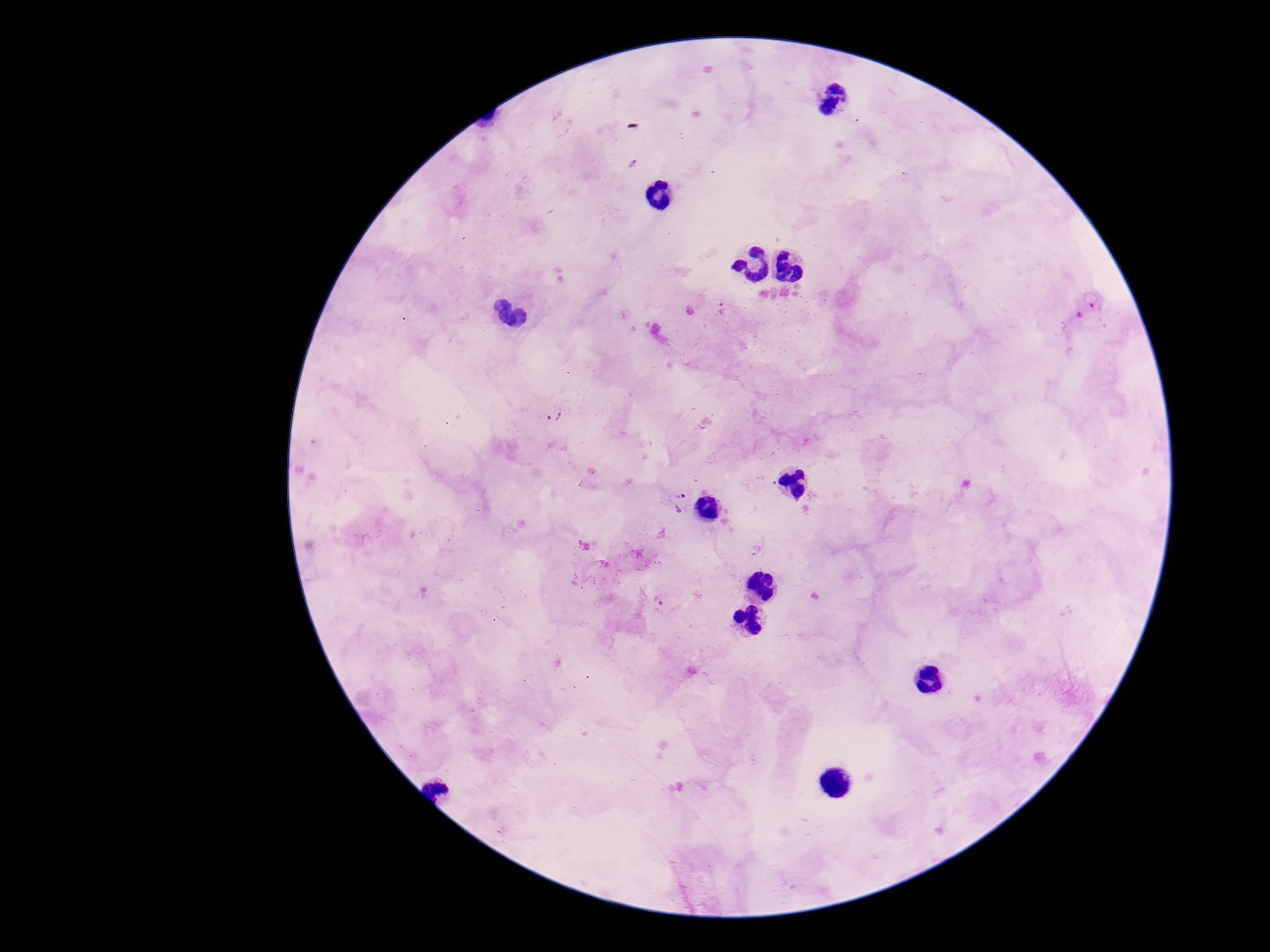

Approximate object centers, in pixels from the top-left corner. Plasmodium parasite locations: (x=633, y=165), (x=1093, y=298), (x=726, y=314), (x=555, y=416), (x=678, y=501), (x=660, y=602). Smartphone photograph taken through the microscope eyepiece. Thick peripheral-blood smear. Single field of view. Patient malaria status: infected. 100x magnification. Giemsa-stained preparation. Image is 1270×952 pixels.